Assess for Plasmodium parasites.
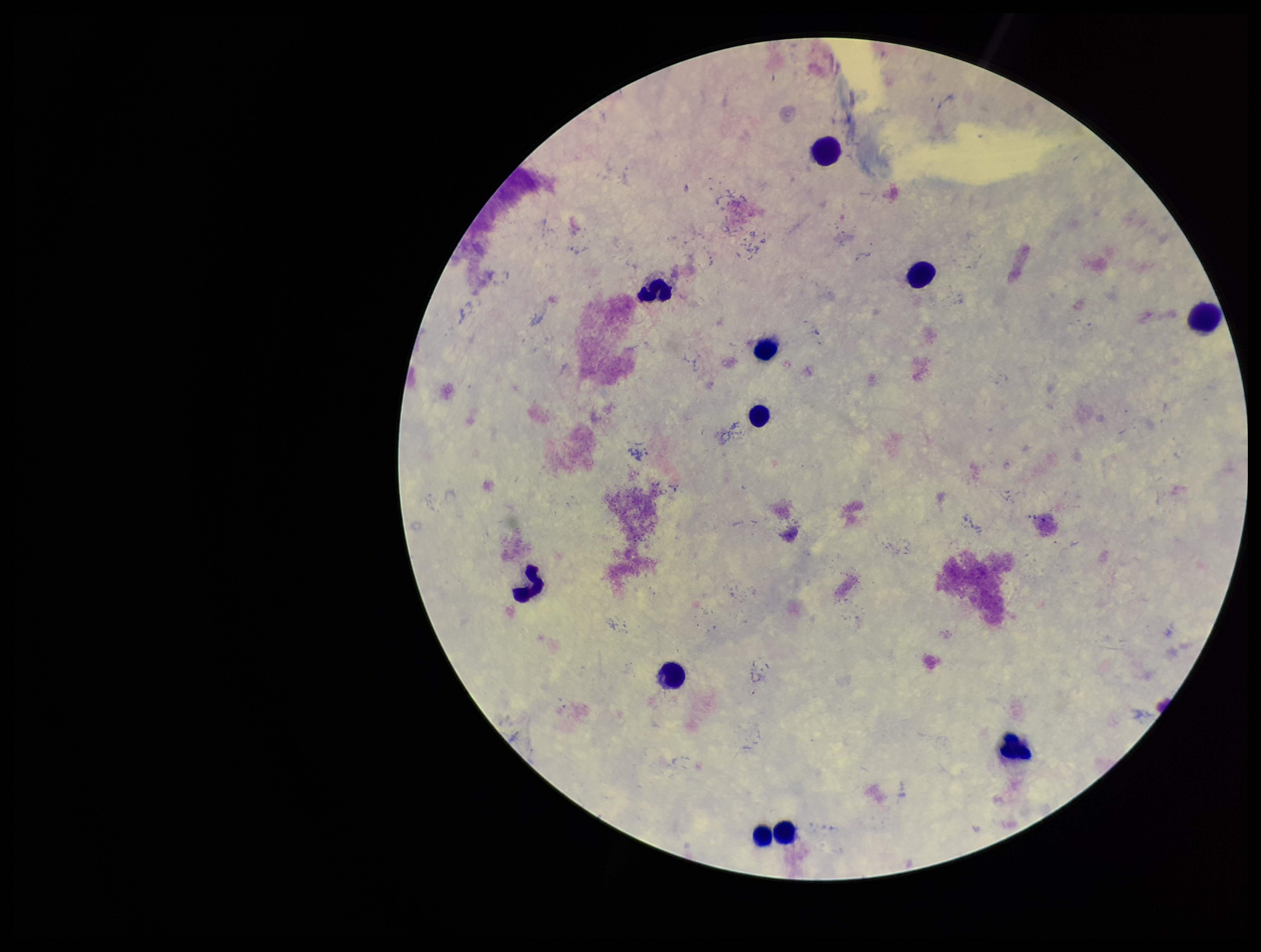
None detected.

Image is 1261×952 pixels. Preparation: thick blood smear. Leukocyte count: 11. Parasite count: 0. Photographed through the microscope eyepiece with a smartphone camera. Giemsa stain. Single field of view. Patient malaria status: negative.